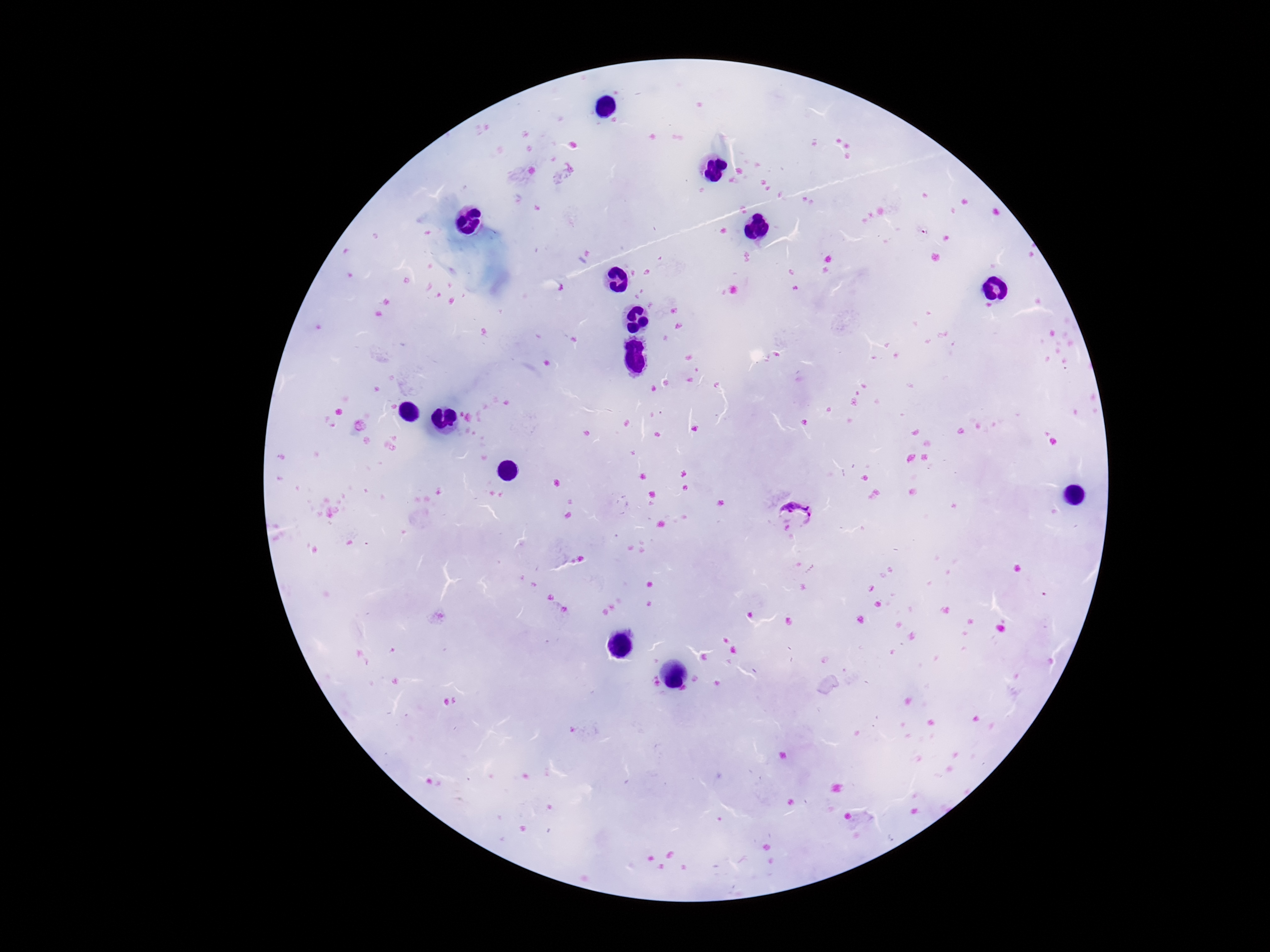

field of view = one from this slide
magnification = 100x
Plasmodium parasite locations = approximate object centers, in pixels from the top-left corner: (x=794, y=516)
stain = Giemsa
patient malaria status = infected
image size = 1270×952 pixels
preparation = thick blood smear
capture = smartphone camera through the microscope eyepiece